Point out each malaria parasite.
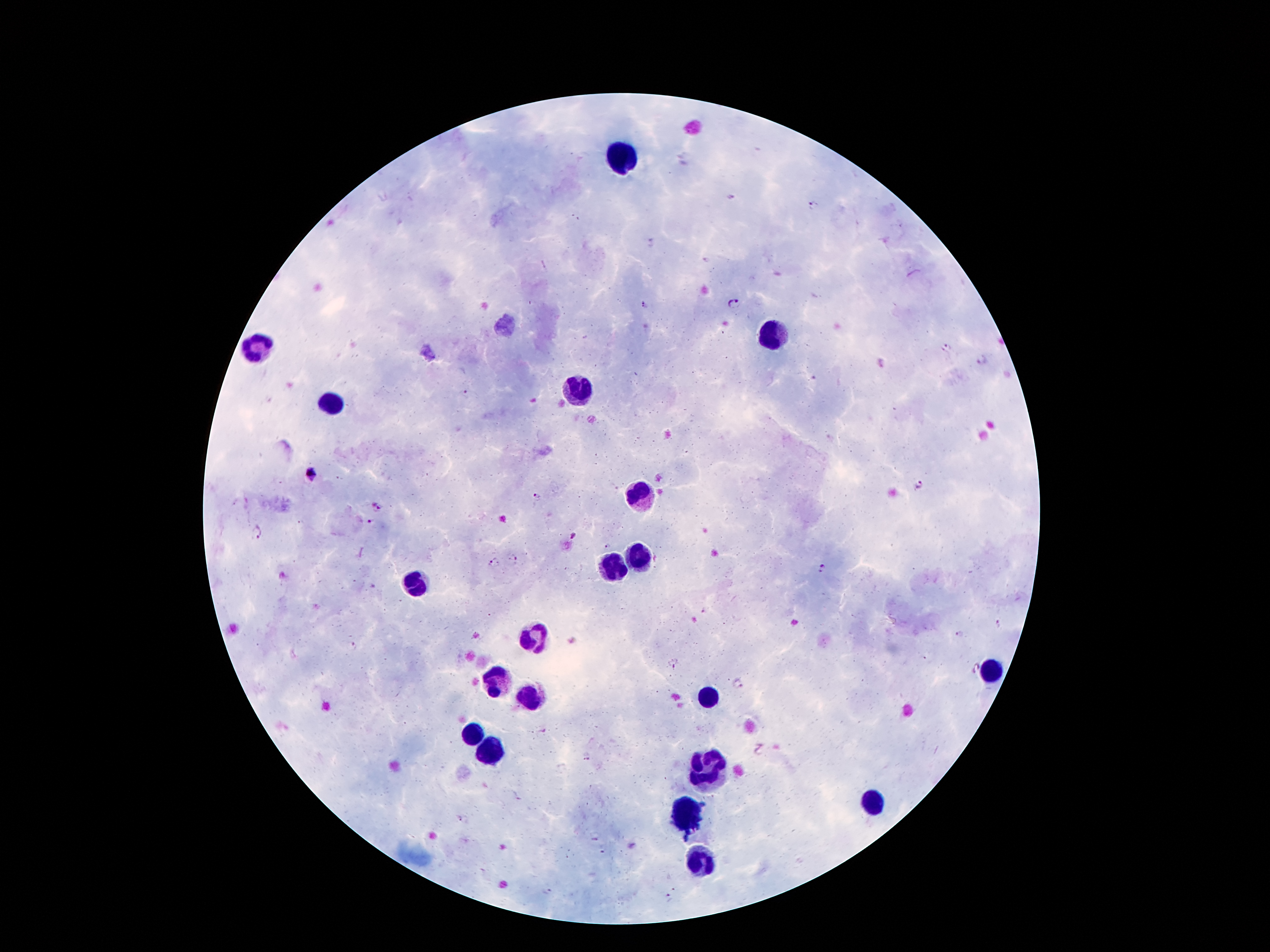
Approximate object centers, in pixels from the top-left corner.
Malaria parasites: (x=813, y=206), (x=651, y=243), (x=735, y=303), (x=645, y=305), (x=946, y=348), (x=983, y=360), (x=465, y=394), (x=310, y=475), (x=921, y=487), (x=537, y=497), (x=379, y=508), (x=369, y=522), (x=259, y=534), (x=574, y=538), (x=512, y=559), (x=493, y=562), (x=823, y=568), (x=998, y=625), (x=959, y=635), (x=353, y=646), (x=674, y=664), (x=974, y=670), (x=738, y=683), (x=587, y=757), (x=548, y=893), (x=669, y=898).

Leukocyte locations: (x=619, y=160), (x=772, y=338), (x=255, y=348), (x=579, y=390), (x=333, y=405), (x=638, y=495), (x=638, y=558), (x=612, y=569), (x=415, y=589), (x=531, y=637), (x=993, y=673), (x=497, y=679), (x=529, y=698), (x=709, y=698), (x=470, y=733), (x=491, y=753), (x=711, y=774), (x=873, y=803), (x=686, y=812), (x=699, y=863). 100x magnification. One field from this slide. Patient malaria status: positive for Plasmodium falciparum. Image is 1270×952 pixels. Thick blood smear. Smartphone photograph taken through the microscope eyepiece. Giemsa-stained preparation.